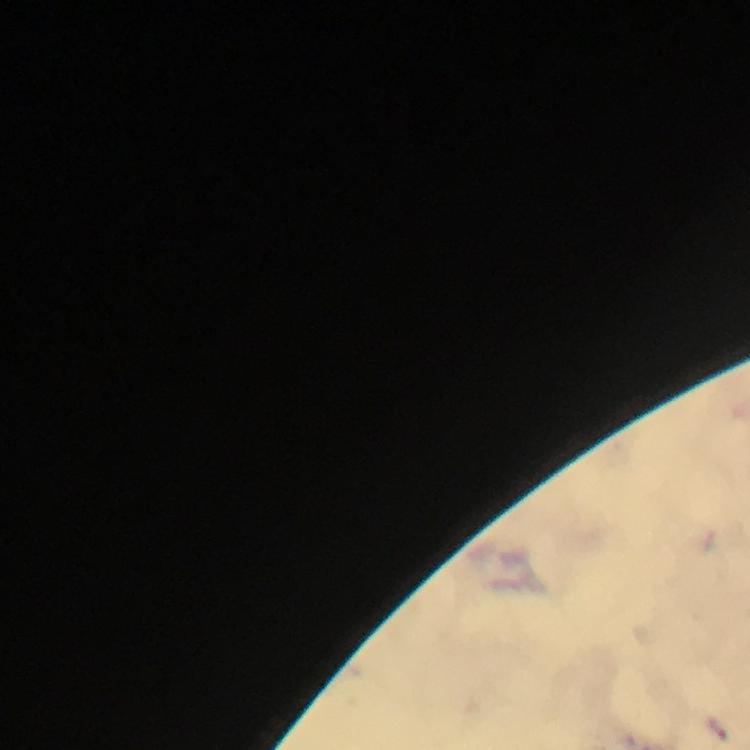

immersion oil = used
Plasmodium parasite locations = approximate centers as [x, y] in pixels: [715, 731]
image size = 750×750 pixels
context = from a malaria diagnostic workup
preparation = thick blood smear
cropped from = a single field of view
capture = smartphone photograph through a microscope
stain = Giemsa
magnification = 100x